Report the malaria status of this cell.
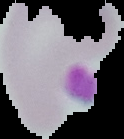
It is uninfected.

Image is 124×139 pixels. From a thin blood smear. Cell region segmented out of the field of view; the surrounding area is masked to black.